Report the malaria status of this cell.
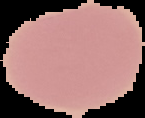

It is uninfected.

Summary:
  - Image size: 145×118 pixels
  - Preparation: thin blood film
  - Image type: segmented cell region with the area outside set to black